State which parasite is depicted.
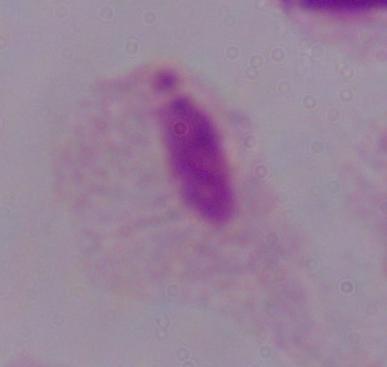
A trichomonad.

modality: micrograph
magnification: 1000x